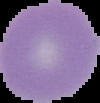

image_type: cell region segmented out of the field of view; surrounding area masked to black
preparation: thin blood smear
malaria_status: uninfected
image_size: 100×103 pixels